Classify this cell by malaria status.
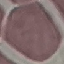

Uninfected.

Automatically extracted cell patch, resized to 64 × 64 pixels. Acquired by smartphone through the microscope eyepiece. Thin blood smear. Giemsa-stained preparation.